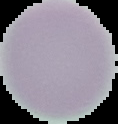

Segmented cell region on a black background. Malaria status: uninfected. Image is 118×124 pixels. From a thin blood smear.